Describe the morphology of the erythrocytes.
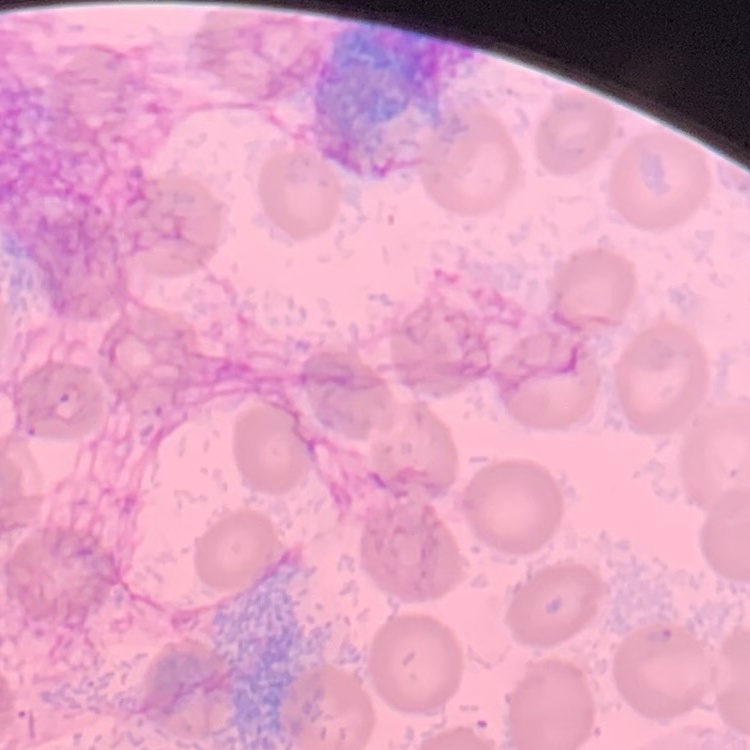

They show no rouleaux formation.

{
  "image_type": "square crop of a larger photomicrograph",
  "stain": "Field's or Giemsa",
  "preparation": "thin peripheral smear"
}